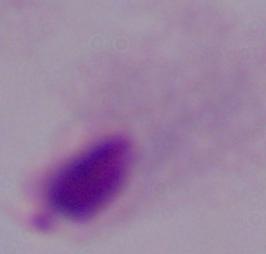

Summary:
  - Identification: trichomonad
  - Modality: photomicrograph
  - Magnification: 1000x